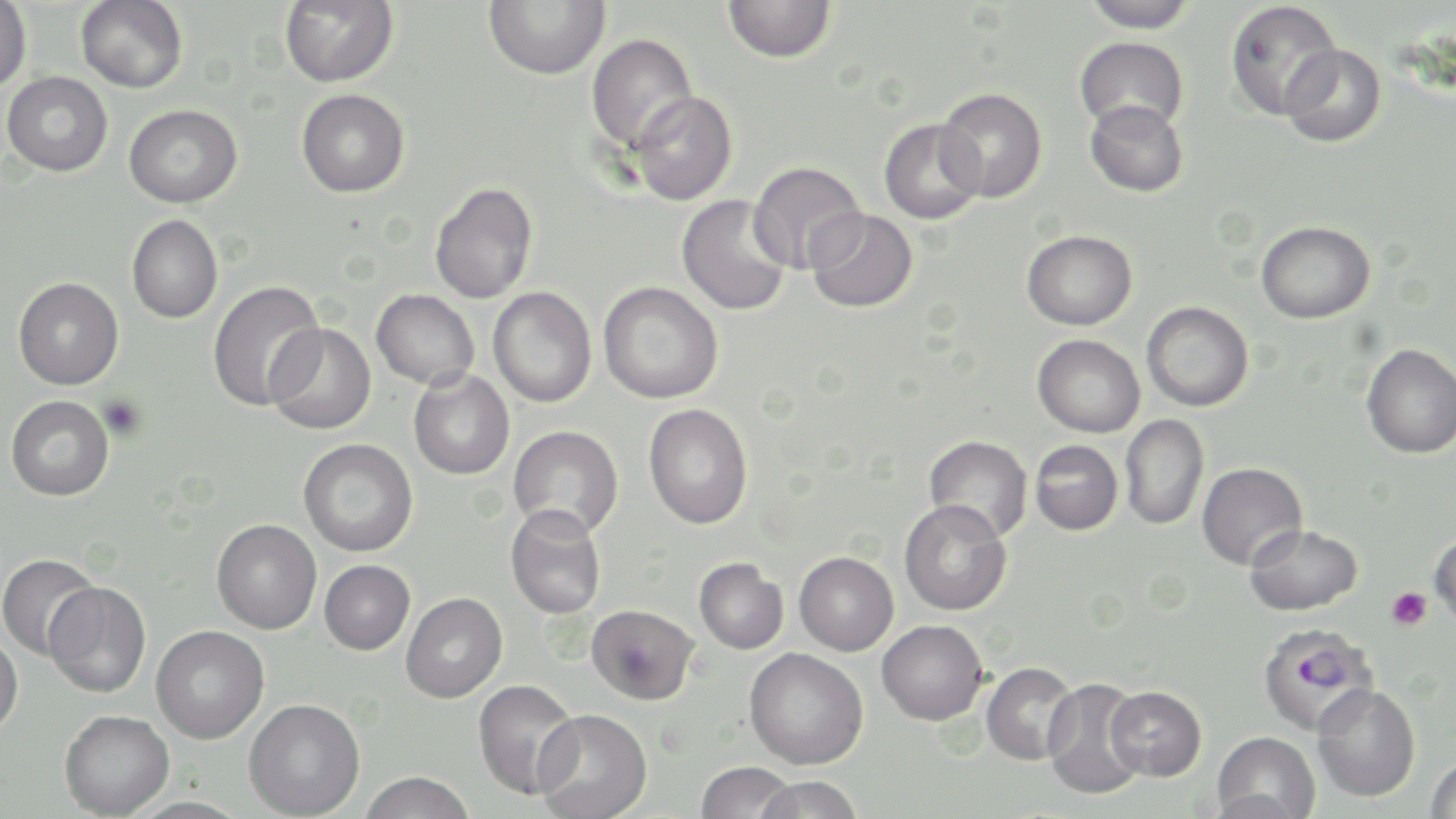
Summary:
  - Coordinate format: approximate bounding boxes as (x1,y1)-(x2,y2) corner pairs in pixels
  - Plasmodium falciparum-infected red blood cell locations: (1258,623)-(1380,737)
  - Uninfected red blood cell locations: (76,0)-(188,93), (279,0)-(398,88), (483,0)-(610,80), (723,0)-(835,63), (1081,0)-(1199,33), (0,1)-(32,91), (1225,1)-(1342,120), (586,33)-(697,154), (1075,36)-(1189,134), (1280,44)-(1387,148), (3,71)-(113,176), (936,88)-(1047,203), (296,89)-(409,197), (628,91)-(737,206), (1085,100)-(1188,197), (124,104)-(242,209), (878,118)-(985,224), (748,161)-(866,274), (429,182)-(538,304), (677,195)-(792,316), (806,208)-(918,313), (126,215)-(223,323), (1256,221)-(1375,323), (1022,230)-(1137,330), (13,277)-(124,390), (207,280)-(325,410), (598,281)-(723,404), (488,287)-(597,408), (371,289)-(479,389), (1142,301)-(1253,412), (265,323)-(376,435), (1032,334)-(1145,438), (1361,343)-(1456,459), (409,370)-(514,480), (6,395)-(114,501), (643,404)-(752,529), (1120,414)-(1209,530), (508,424)-(623,539), (924,436)-(1033,542), (298,438)-(418,556), (1030,440)-(1123,535), (1196,462)-(1307,570), (899,499)-(1012,616), (505,505)-(606,619), (212,519)-(322,634), (1244,523)-(1362,616), (1430,534)-(1456,631), (794,552)-(898,655), (0,553)-(101,660), (694,557)-(788,654), (319,560)-(415,655), (44,581)-(151,698), (401,592)-(507,703), (587,604)-(699,705), (877,620)-(987,724), (151,625)-(269,743), (0,632)-(23,737), (744,648)-(868,769), (981,662)-(1079,765), (1042,677)-(1150,799), (473,679)-(582,800), (1311,684)-(1421,801), (1106,685)-(1207,780), (244,698)-(365,819), (59,709)-(174,818), (533,709)-(653,819), (1211,731)-(1320,819), (1425,756)-(1456,819), (695,762)-(798,818), (359,771)-(476,818), (753,775)-(865,819), (123,797)-(253,818)
  - Platelet locations: (100,396)-(146,439), (1387,587)-(1431,630)
  - Slide-level diagnosis: Plasmodium falciparum
  - Stain: May-Grünwald-Giemsa
  - Preparation: thin blood film
  - Image size: 1456×819 pixels
  - Modality: optical microscopy
  - Magnification: 1000x
  - Field of view: single